Name the parasite shown.
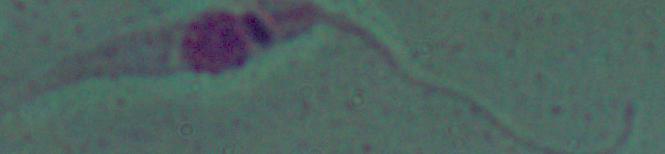
This is Leishmania.

1000x magnification. Micrograph.